Give the position of every Plasmodium parasite visible.
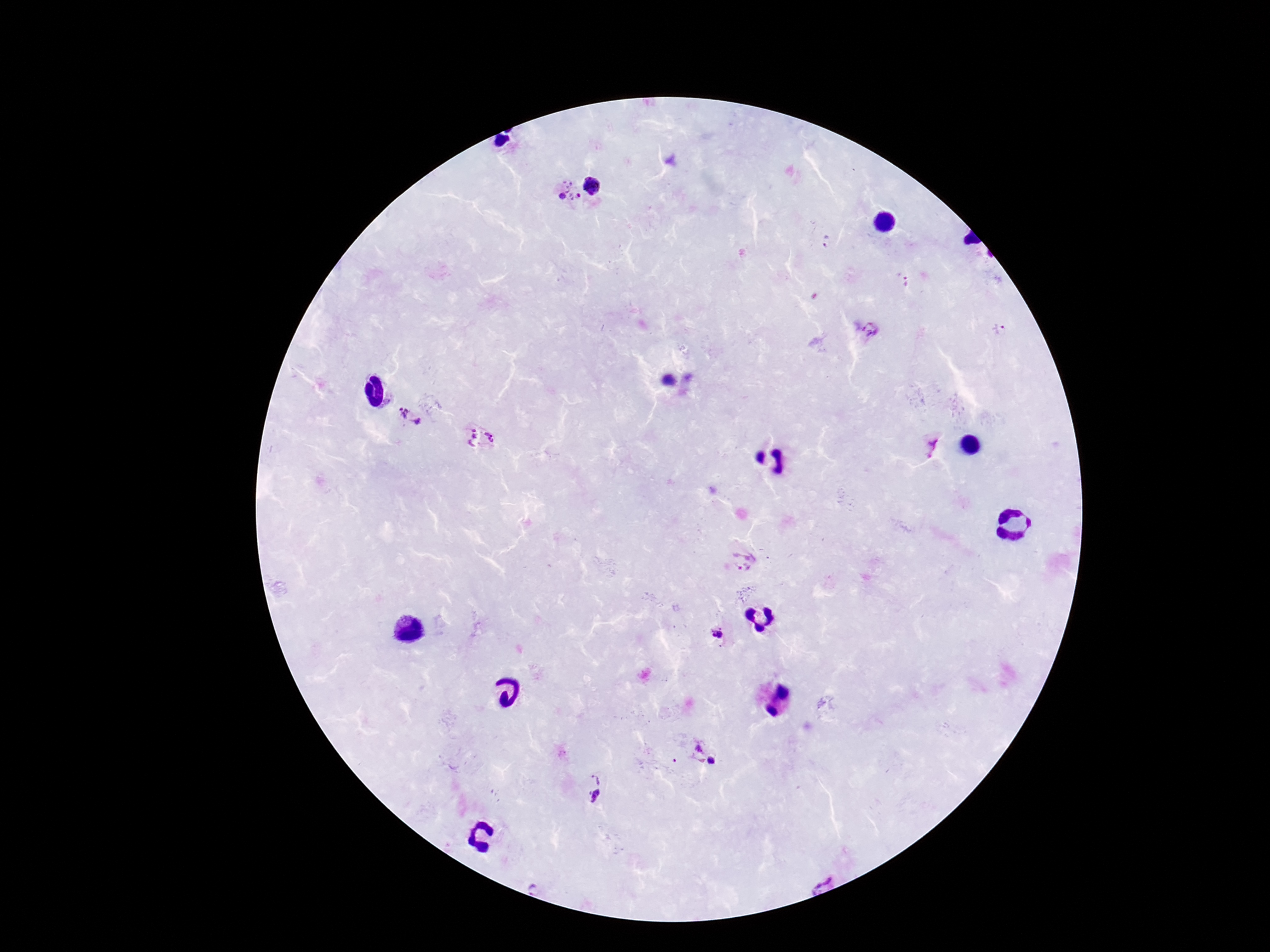

Approximate centers as (x, y) in pixels.
Plasmodium parasites: (592, 185), (568, 190), (827, 241), (905, 281), (1000, 329), (866, 330), (409, 416), (480, 438), (933, 445), (746, 560), (715, 633), (694, 748), (717, 761), (596, 776), (595, 796).

capture = smartphone camera through the microscope eyepiece
preparation = thick blood film
patient malaria status = positive
image size = 1270×952 pixels
field of view = one from this slide
magnification = 100x
stain = Giemsa